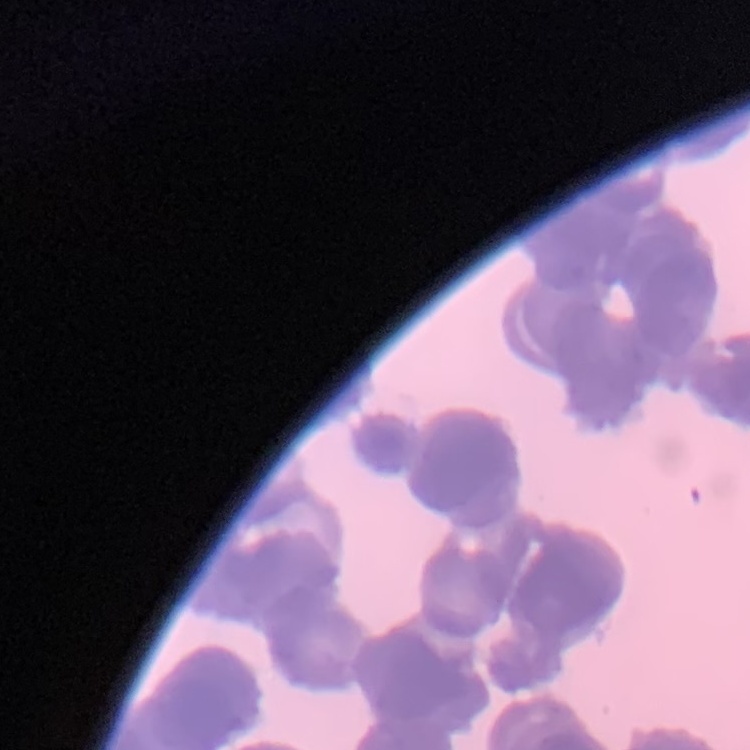 The red blood cells show rouleaux formation. Field's or Giemsa stain. Square crop of a larger photomicrograph. Thin peripheral smear.